Name the parasite shown.
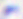

Toxoplasma gondii.

{
  "magnification": "400x",
  "modality": "photomicrograph"
}